Describe the morphology of the erythrocytes.
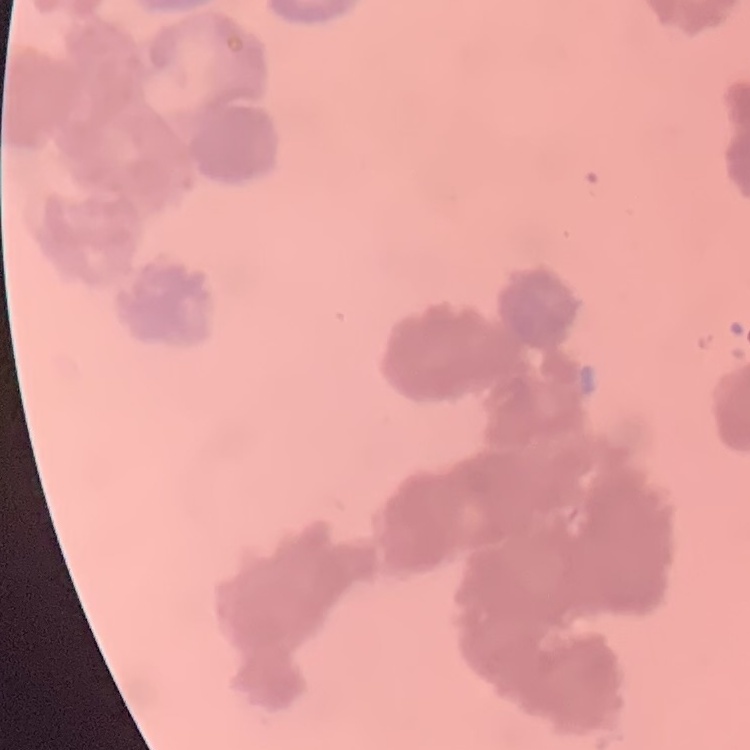

They show rouleaux formation.

Field's or Giemsa stain. One tile cut from a larger photomicrograph. Thin blood smear.